State the blood parasite species.
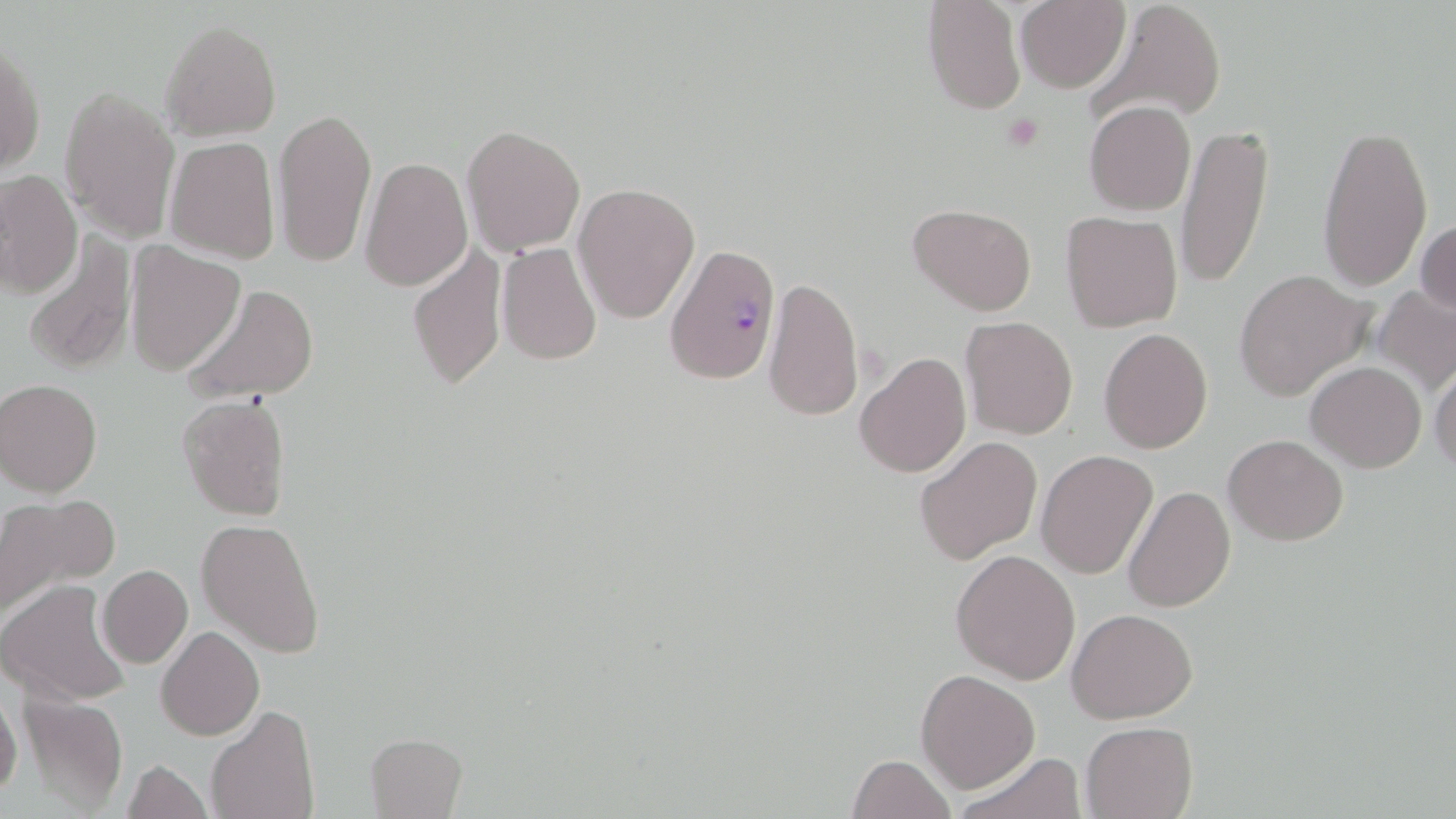

Plasmodium falciparum.

Approximate bounding boxes as named x1/y1/x2/y2 corners in pixels. Plasmodium falciparum-infected red blood cell locations: (x1=664, y1=243, x2=780, y2=384). Uninfected red blood cell locations: (x1=1087, y1=0, x2=1227, y2=128), (x1=922, y1=1, x2=1026, y2=114), (x1=1014, y1=1, x2=1132, y2=92), (x1=160, y1=19, x2=281, y2=142), (x1=1, y1=44, x2=44, y2=177), (x1=59, y1=85, x2=181, y2=243), (x1=1084, y1=100, x2=1197, y2=216), (x1=272, y1=107, x2=377, y2=267), (x1=1316, y1=119, x2=1433, y2=292), (x1=1176, y1=122, x2=1273, y2=290), (x1=460, y1=124, x2=586, y2=256), (x1=165, y1=135, x2=281, y2=265), (x1=359, y1=157, x2=473, y2=290), (x1=0, y1=170, x2=82, y2=300), (x1=573, y1=182, x2=701, y2=325), (x1=909, y1=204, x2=1037, y2=315), (x1=1059, y1=211, x2=1183, y2=331), (x1=1415, y1=218, x2=1455, y2=320), (x1=23, y1=234, x2=137, y2=377), (x1=407, y1=239, x2=506, y2=391), (x1=125, y1=242, x2=245, y2=376), (x1=495, y1=242, x2=602, y2=366), (x1=1234, y1=270, x2=1374, y2=401), (x1=762, y1=276, x2=865, y2=422), (x1=181, y1=283, x2=320, y2=403), (x1=1372, y1=284, x2=1456, y2=396), (x1=959, y1=316, x2=1078, y2=440), (x1=1099, y1=327, x2=1213, y2=452), (x1=854, y1=351, x2=972, y2=479), (x1=1428, y1=357, x2=1456, y2=477), (x1=1306, y1=361, x2=1426, y2=472), (x1=1, y1=379, x2=102, y2=497), (x1=177, y1=393, x2=292, y2=522), (x1=1223, y1=433, x2=1347, y2=545), (x1=915, y1=436, x2=1042, y2=564), (x1=1035, y1=449, x2=1158, y2=579), (x1=1122, y1=486, x2=1236, y2=612), (x1=0, y1=493, x2=119, y2=623), (x1=196, y1=518, x2=325, y2=658), (x1=950, y1=548, x2=1081, y2=684), (x1=98, y1=564, x2=193, y2=668), (x1=0, y1=581, x2=132, y2=707), (x1=1068, y1=607, x2=1197, y2=723), (x1=156, y1=626, x2=264, y2=741), (x1=915, y1=669, x2=1040, y2=794), (x1=16, y1=691, x2=130, y2=815), (x1=0, y1=692, x2=22, y2=802), (x1=207, y1=704, x2=318, y2=819), (x1=1080, y1=720, x2=1199, y2=818), (x1=366, y1=732, x2=467, y2=817), (x1=957, y1=752, x2=1086, y2=819), (x1=846, y1=754, x2=958, y2=818), (x1=122, y1=759, x2=211, y2=819). Platelet locations: (x1=1001, y1=112, x2=1046, y2=153). Light microscopy. May-Grünwald-Giemsa stain. Thin blood smear. Image is 1456×819 pixels. One field of a larger specimen. 1000x magnification.